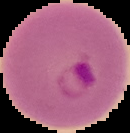

malaria status = parasitized
image size = 130×133 pixels
image type = segmented cell region with the area outside set to black
preparation = thin blood smear